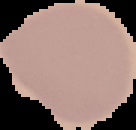

Summary:
  - Image size: 136×130 pixels
  - Image type: segmented cell region on a black background
  - Result: no Plasmodium parasites seen
  - Preparation: thin blood film